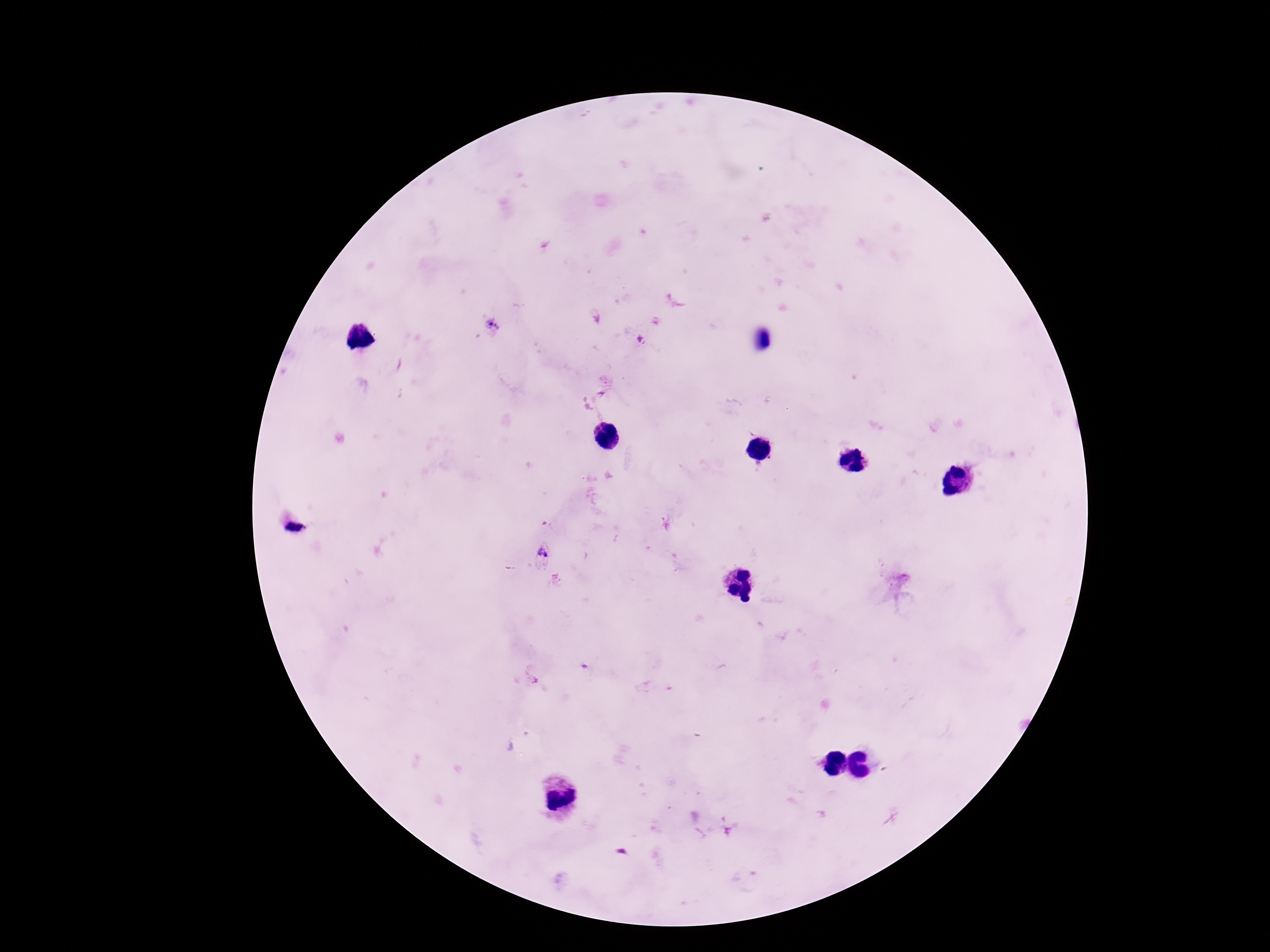
Approximate object centers, in pixels from the top-left corner. Plasmodium parasite locations: (x=493, y=326), (x=295, y=530), (x=543, y=553). Patient malaria status: positive. Giemsa stain. Thick blood film. 100x magnification. One field from this slide. Photographed through the microscope eyepiece with a smartphone camera. Image is 1270×952 pixels.